Report the malaria status of this cell.
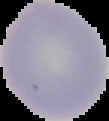
It is uninfected.

preparation = thin blood smear
image type = cell region segmented out of the field of view; surrounding area masked to black
image size = 109×121 pixels